Identify the parasite.
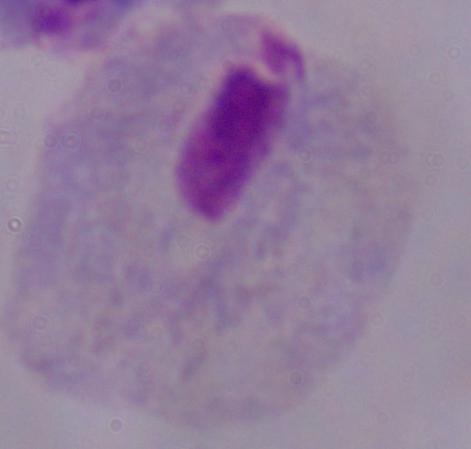
A trichomonad.

magnification = 1000x
modality = photomicrograph